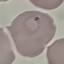

Result: malaria parasites detected. Acquired by smartphone through the microscope eyepiece. Cell patch, automatically extracted from a larger field of view and resized to 64 × 64 pixels. Giemsa-stained preparation. Thin smear of blood.